Report the malaria status of this cell.
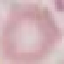

Uninfected.

Giemsa-stained preparation. Automatically extracted cell patch, resized to 64 × 64 pixels. Acquired by smartphone through the microscope eyepiece. Thin blood smear.